Comment on the morphology of the red blood cells.
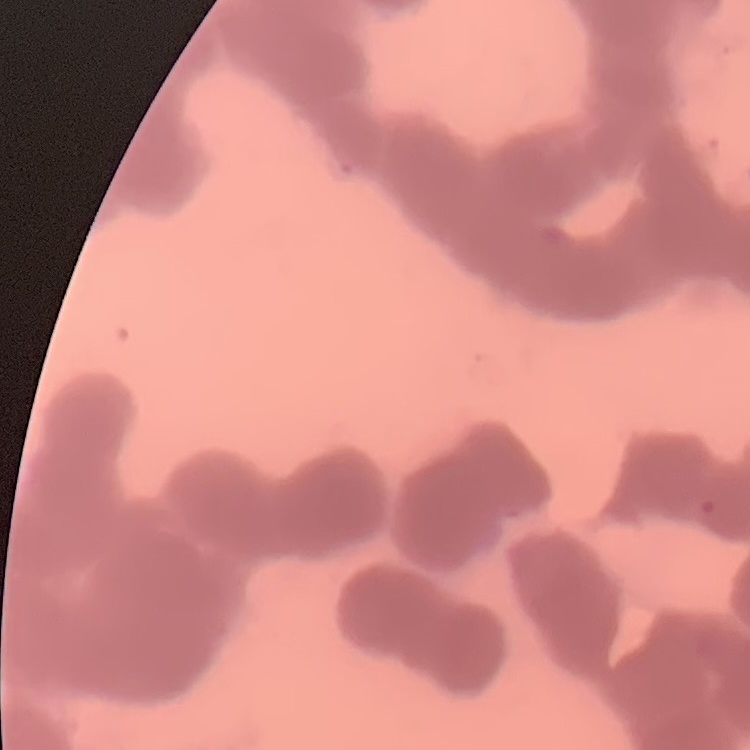

They show rouleaux formation.

Thin blood film. One tile cut from a larger photomicrograph. Field's or Giemsa stain.